Assess this cell for malaria.
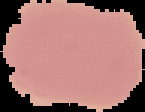

It is uninfected.

image type = segmented cell region with the area outside set to black
preparation = thin blood smear
image size = 145×112 pixels